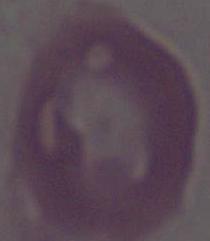
Summary:
  - Magnification: 1000x
  - Identification: erythrocyte
  - Modality: micrograph